Locate every blood parasite and identify its species.
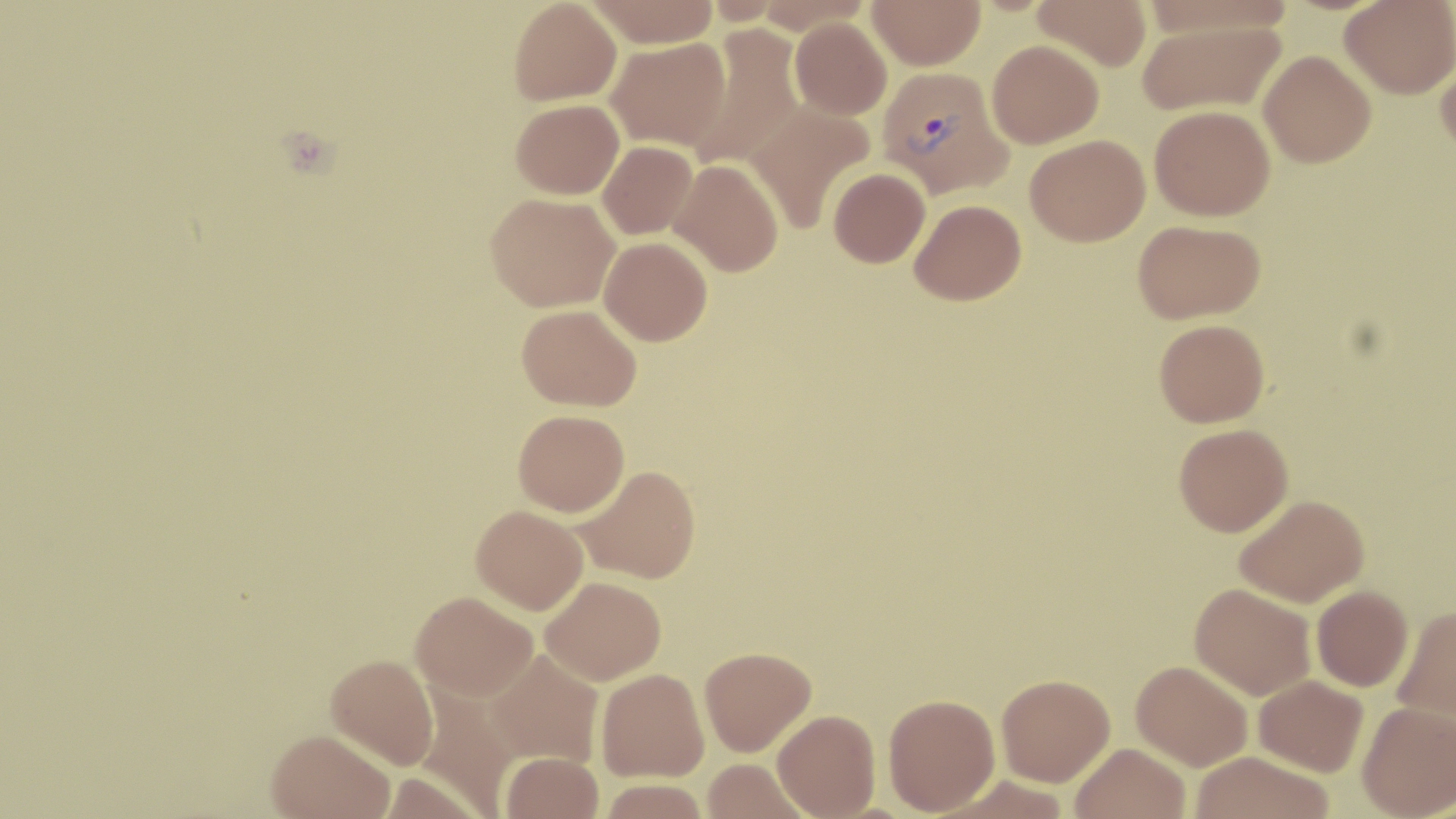
Approximate bounding boxes as named x1/y1/x2/y2 corners in pixels.
Plasmodium vivax-infected red blood cells: (x1=876, y1=64, x2=1012, y2=198).
No Plasmodium falciparum, Plasmodium ovale, Plasmodium malariae, Babesia divergens, or Trypanosoma brucei observed.

Uninfected red blood cell locations: (x1=509, y1=0, x2=621, y2=105), (x1=584, y1=0, x2=721, y2=47), (x1=867, y1=0, x2=985, y2=70), (x1=1033, y1=0, x2=1152, y2=71), (x1=1340, y1=0, x2=1456, y2=99), (x1=1137, y1=16, x2=1288, y2=116), (x1=790, y1=18, x2=892, y2=120), (x1=685, y1=26, x2=804, y2=170), (x1=605, y1=38, x2=730, y2=150), (x1=987, y1=39, x2=1104, y2=148), (x1=1435, y1=48, x2=1456, y2=159), (x1=1259, y1=50, x2=1376, y2=168), (x1=511, y1=99, x2=624, y2=199), (x1=746, y1=100, x2=876, y2=233), (x1=1149, y1=105, x2=1275, y2=221), (x1=1025, y1=135, x2=1150, y2=246), (x1=597, y1=141, x2=697, y2=240), (x1=668, y1=158, x2=784, y2=277), (x1=828, y1=167, x2=930, y2=268), (x1=486, y1=193, x2=619, y2=312), (x1=910, y1=199, x2=1026, y2=305), (x1=1132, y1=219, x2=1265, y2=324), (x1=599, y1=236, x2=712, y2=346), (x1=516, y1=304, x2=641, y2=410), (x1=1154, y1=319, x2=1269, y2=427), (x1=513, y1=409, x2=629, y2=517), (x1=1173, y1=422, x2=1293, y2=536), (x1=575, y1=465, x2=701, y2=584), (x1=1234, y1=493, x2=1370, y2=608), (x1=471, y1=504, x2=589, y2=614), (x1=541, y1=576, x2=666, y2=685), (x1=1190, y1=582, x2=1316, y2=700), (x1=1311, y1=585, x2=1413, y2=691), (x1=411, y1=591, x2=538, y2=702), (x1=1392, y1=605, x2=1456, y2=732), (x1=699, y1=646, x2=816, y2=756), (x1=486, y1=649, x2=604, y2=768), (x1=325, y1=654, x2=438, y2=770), (x1=1131, y1=660, x2=1253, y2=770), (x1=596, y1=668, x2=709, y2=781), (x1=996, y1=673, x2=1115, y2=786), (x1=1253, y1=674, x2=1368, y2=776), (x1=883, y1=694, x2=1000, y2=815), (x1=1357, y1=701, x2=1456, y2=818), (x1=772, y1=709, x2=880, y2=818), (x1=266, y1=729, x2=394, y2=819), (x1=1071, y1=743, x2=1191, y2=819), (x1=500, y1=751, x2=604, y2=818), (x1=1190, y1=751, x2=1334, y2=819), (x1=701, y1=759, x2=812, y2=819), (x1=598, y1=778, x2=710, y2=818). Slide-level diagnosis: Plasmodium vivax. 1000x magnification. Image is 1456×819 pixels. One field of a larger specimen. Optical microscopy. May-Grünwald-Giemsa-stained preparation. Thin blood smear.